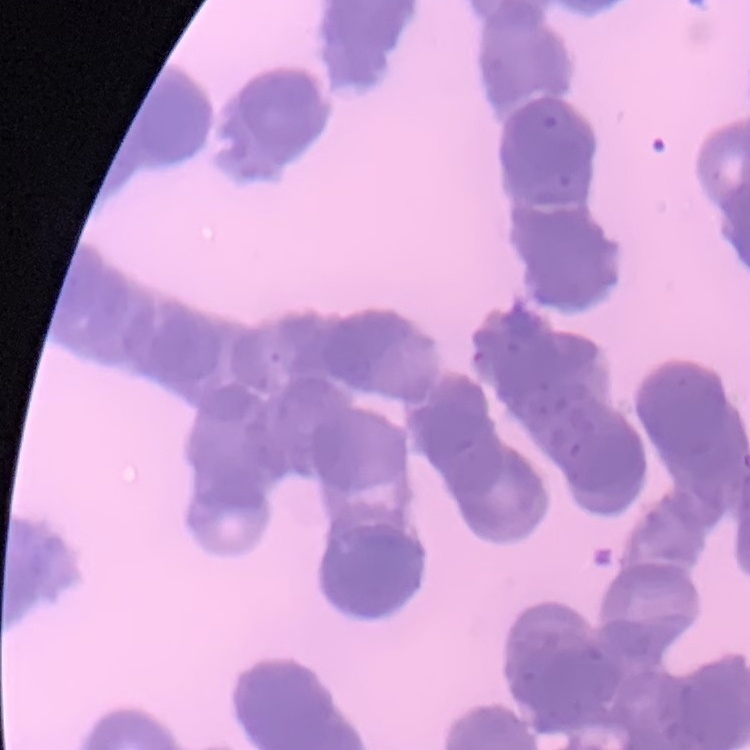
The erythrocytes exhibit rouleaux formation. Stained with either Field's or Giemsa. Thin blood film. One tile cut from a larger photomicrograph.